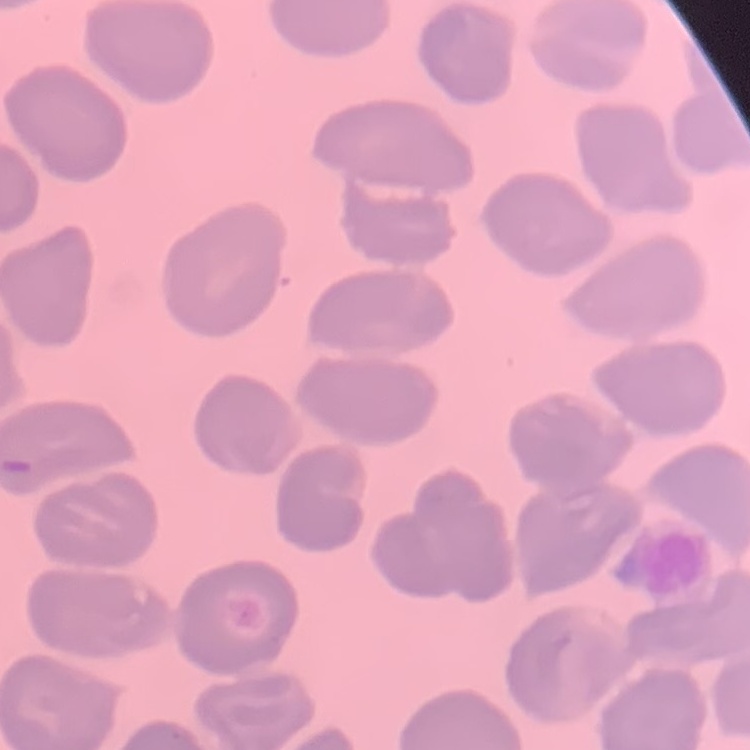
Summary:
  - Erythrocyte morphology: no rouleaux formation
  - Stain: Field's or Giemsa
  - Image type: one tile cut from a larger photomicrograph
  - Preparation: thin peripheral smear